Locate and identify every blood parasite.
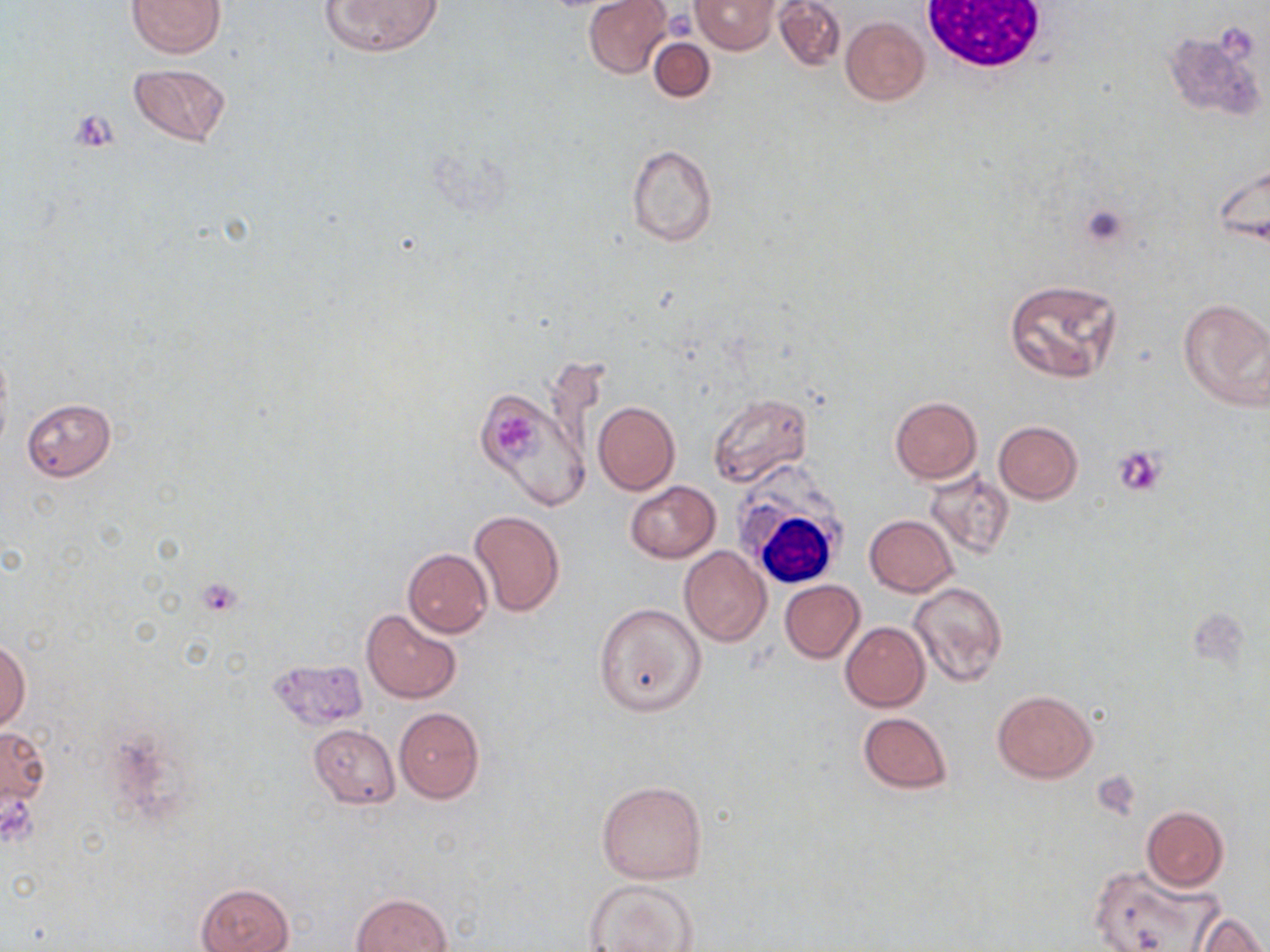

No blood parasites seen.

slide-level diagnosis = negative for blood parasites
modality = optical microscopy
white blood cell locations = approximate bounding boxes as [x1, y1, x2, y2] in pixels: [915, 1, 1055, 74], [731, 479, 852, 593]
field of view = single
image size = 1270×952 pixels
platelet locations = approximate bounding boxes as [x1, y1, x2, y2] in pixels: [664, 9, 694, 40], [496, 413, 543, 462], [1113, 445, 1167, 497], [194, 577, 242, 619], [1093, 773, 1138, 817]
uninfected red blood cell locations = approximate bounding boxes as [x1, y1, x2, y2] in pixels: [125, 0, 226, 57], [321, 0, 441, 57], [583, 0, 674, 78], [691, 0, 780, 53], [772, 0, 846, 73], [840, 16, 929, 105], [649, 37, 715, 102], [129, 62, 231, 147], [626, 143, 717, 248], [1003, 277, 1122, 385], [1178, 297, 1270, 411], [473, 390, 587, 510], [707, 393, 813, 489], [888, 396, 983, 483], [22, 398, 116, 481], [594, 401, 679, 495], [993, 420, 1083, 503], [925, 469, 1016, 559], [624, 480, 720, 562], [469, 510, 564, 616], [865, 515, 957, 596], [720, 533, 838, 638], [678, 547, 772, 647], [403, 549, 492, 637], [780, 581, 864, 663], [909, 581, 1008, 688], [594, 601, 705, 717], [361, 609, 462, 703], [840, 621, 930, 711], [0, 639, 31, 733], [268, 658, 368, 730], [991, 688, 1098, 783], [395, 707, 484, 803], [857, 712, 953, 794], [1, 721, 50, 826], [307, 723, 400, 808], [597, 780, 707, 884], [1141, 806, 1229, 891], [1089, 864, 1218, 951], [581, 878, 699, 951], [197, 883, 293, 952], [351, 892, 452, 952], [1193, 911, 1267, 951]
preparation = thin blood smear
stain = May-Grünwald-Giemsa
magnification = 1000x